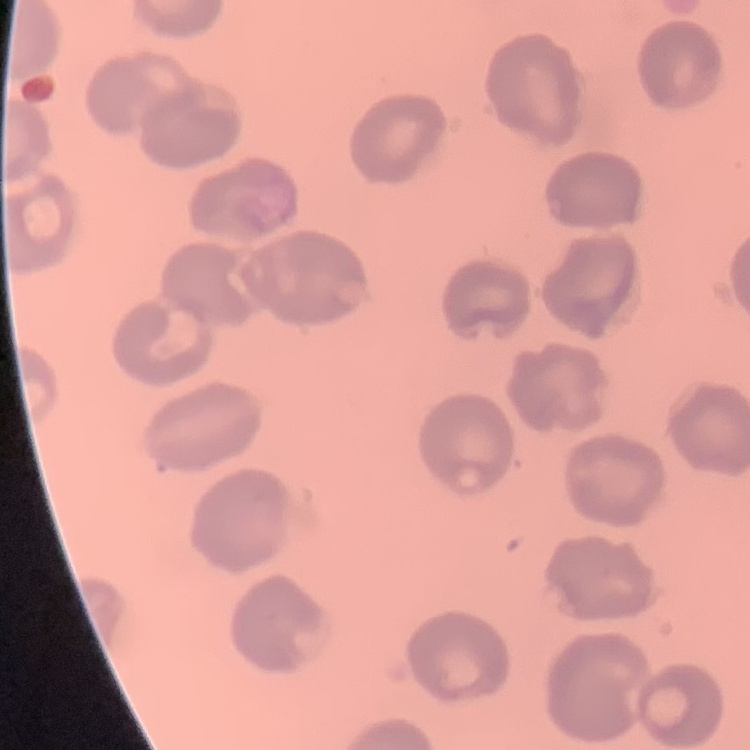
Summary:
  - Red blood cell morphology: no rouleaux formation
  - Image type: square crop of a larger photomicrograph
  - Stain: Field's or Giemsa
  - Preparation: thin peripheral smear